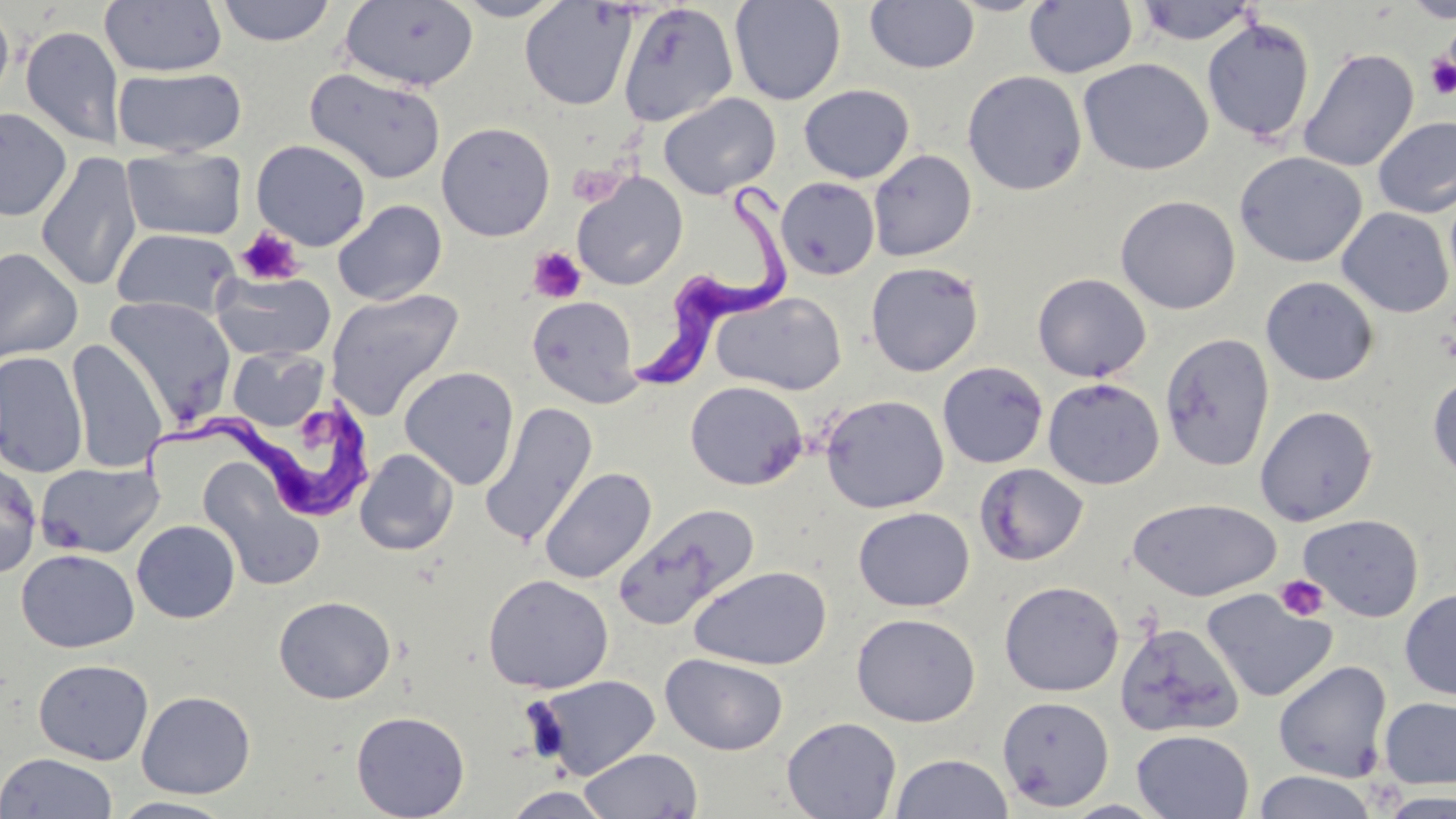
Approximate bounding boxes as [x1, y1, x2, y2] in pixels. Uninfected red blood cell locations: [215, 0, 337, 46], [339, 0, 480, 92], [452, 0, 568, 21], [729, 0, 846, 105], [1400, 0, 1456, 24], [100, 1, 227, 76], [520, 1, 637, 111], [865, 1, 980, 74], [1023, 1, 1138, 78], [1134, 1, 1259, 46], [0, 3, 15, 109], [618, 3, 739, 127], [1201, 17, 1316, 143], [20, 25, 126, 150], [1297, 47, 1419, 172], [1078, 57, 1214, 176], [112, 67, 247, 157], [305, 68, 447, 184], [962, 70, 1087, 196], [798, 84, 914, 184], [658, 92, 781, 200], [0, 107, 72, 221], [1373, 115, 1456, 219], [436, 121, 556, 242], [251, 139, 372, 251], [121, 147, 247, 241], [868, 149, 976, 261], [1234, 151, 1367, 268], [36, 152, 142, 292], [572, 173, 688, 290], [775, 177, 880, 280], [1115, 195, 1241, 314], [333, 200, 447, 305], [1337, 207, 1454, 318], [111, 228, 240, 319], [0, 248, 83, 363], [865, 261, 984, 377], [211, 270, 336, 362], [1032, 272, 1152, 382], [1260, 276, 1379, 387], [324, 288, 464, 422], [711, 290, 847, 395], [527, 294, 641, 407], [104, 296, 236, 424], [1160, 332, 1275, 472], [67, 340, 168, 473], [228, 347, 329, 431], [0, 350, 87, 478], [937, 361, 1049, 469], [399, 367, 520, 489], [1427, 371, 1456, 485], [1042, 377, 1164, 490], [684, 381, 808, 490], [820, 394, 949, 514], [480, 402, 598, 546], [1254, 404, 1379, 526], [355, 448, 458, 555], [198, 456, 324, 591], [0, 460, 42, 578], [35, 462, 164, 558], [975, 462, 1089, 565], [539, 467, 657, 584], [1128, 498, 1282, 602], [616, 503, 761, 627], [853, 507, 975, 612], [1298, 513, 1424, 621], [131, 519, 241, 623], [15, 548, 139, 653], [26, 550, 144, 765], [689, 565, 832, 670], [482, 574, 614, 693], [999, 581, 1124, 697], [1399, 587, 1456, 701], [1200, 588, 1338, 703], [273, 595, 396, 704], [851, 613, 981, 727], [1114, 622, 1244, 737], [661, 653, 788, 755], [33, 658, 154, 765], [1272, 660, 1394, 783], [531, 675, 661, 779], [136, 690, 256, 799], [996, 695, 1114, 811], [1378, 696, 1456, 789], [350, 710, 471, 819], [781, 716, 902, 818], [1131, 729, 1254, 818], [579, 747, 703, 819], [0, 752, 118, 819], [890, 753, 1014, 818], [1251, 771, 1380, 819], [501, 787, 616, 818], [109, 796, 238, 818], [1056, 799, 1172, 818]. Platelet locations: [1425, 57, 1456, 99], [236, 225, 305, 286], [528, 246, 586, 303], [1275, 575, 1329, 621]. Trypanosoma brucei locations: [627, 171, 794, 396], [133, 396, 373, 517]. Slide-level diagnosis: Trypanosoma brucei. Thin blood film. May-Grünwald-Giemsa-stained preparation. Single field of view. Image is 1456×819 pixels. 1000x magnification. Optical microscopy.